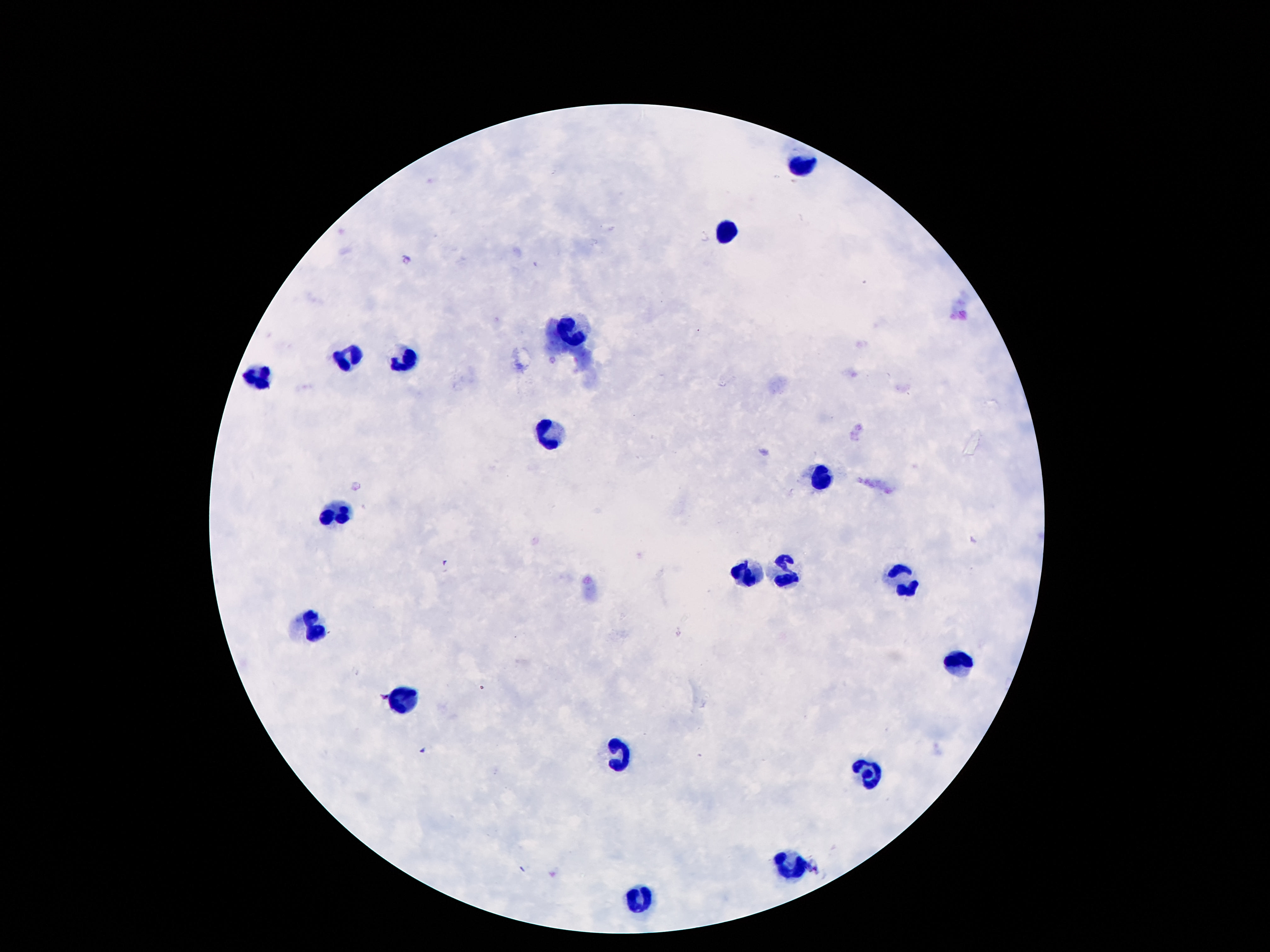
Approximate centers as (x, y) in pixels.
Summary:
  - Leukocyte locations: (806, 167), (726, 230), (573, 331), (350, 356), (405, 362), (262, 374), (548, 437), (817, 480), (339, 517), (745, 574), (784, 574), (901, 585), (313, 628), (962, 662), (401, 701), (616, 756), (868, 777), (792, 865), (640, 895)
  - Image size: 1270×952 pixels
  - Magnification: 100x
  - Capture: smartphone camera through the microscope eyepiece
  - Preparation: thick blood smear
  - Field of view: single
  - Stain: Giemsa
  - Patient malaria status: negative